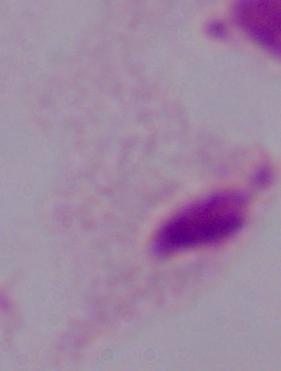 Micrograph. A trichomonad is seen. 1000x magnification.